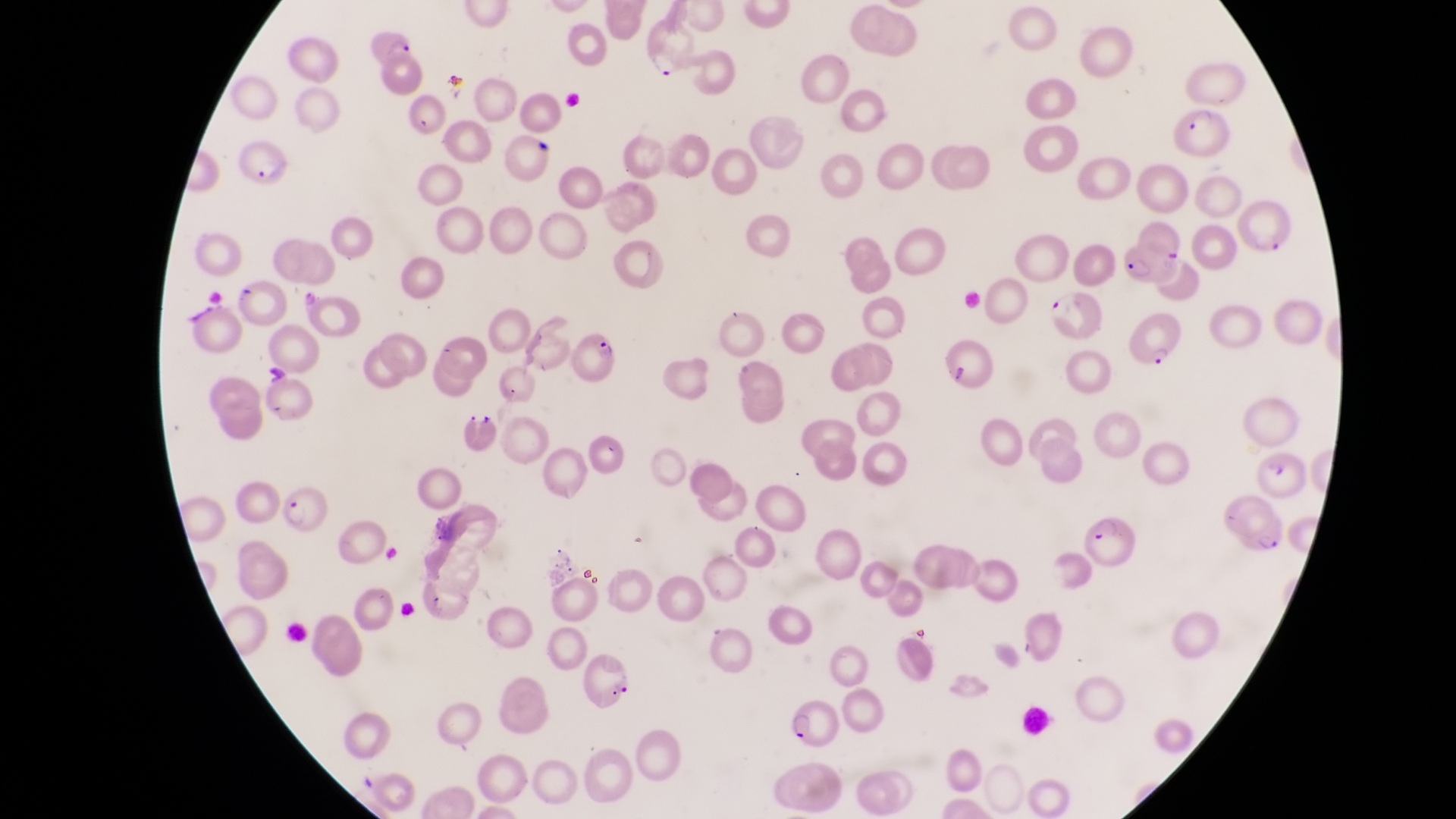
Approximate bounding boxes as [left, top, right, bottom] in pixels.
Summary:
  - Parasitised red blood cell locations: [645, 27, 694, 83], [366, 33, 418, 67], [1169, 103, 1228, 159], [232, 139, 287, 188], [1238, 201, 1296, 257], [1120, 243, 1180, 288], [1118, 312, 1187, 371], [563, 328, 622, 384], [278, 482, 333, 537], [1224, 499, 1288, 559], [1080, 510, 1139, 568], [582, 653, 640, 709], [788, 695, 843, 748]
  - Leukocyte locations: [1015, 700, 1050, 739]
  - Image size: 1456×819 pixels
  - Field of view: single
  - Capture: smartphone photograph through the eyepiece of an Olympus CX-23 microscope
  - Preparation: thin blood smear
  - Country: Uganda
  - Magnification: 1000x